Locate every blood parasite and identify its species.
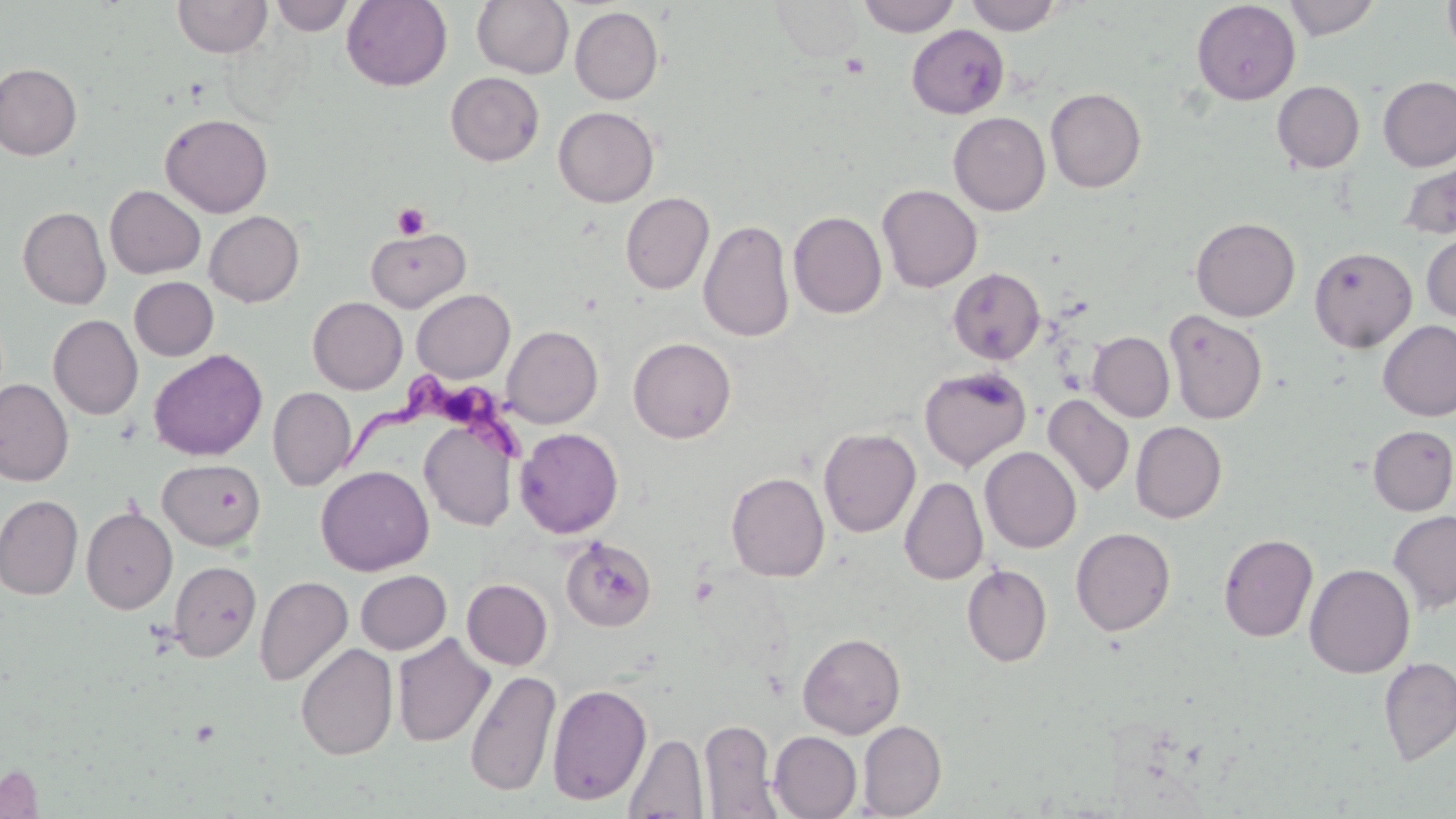

Approximate bounding boxes as [x1, y1, x2, y2] in pixels.
Trypanosoma brucei: [340, 373, 530, 470].
No Plasmodium falciparum, Plasmodium ovale, Plasmodium malariae, Plasmodium vivax, or Babesia divergens observed.

Summary:
  - Uninfected red blood cell locations: [269, 0, 354, 36], [341, 0, 452, 91], [472, 0, 574, 78], [770, 0, 865, 62], [856, 0, 961, 37], [965, 0, 1064, 35], [1283, 0, 1382, 40], [1442, 0, 1456, 60], [172, 1, 272, 58], [1191, 1, 1300, 105], [570, 6, 664, 105], [907, 24, 1009, 118], [0, 62, 82, 161], [445, 72, 545, 166], [1377, 76, 1456, 172], [1272, 81, 1364, 173], [1045, 88, 1146, 192], [553, 106, 659, 207], [948, 112, 1050, 216], [160, 114, 273, 217], [1397, 156, 1456, 240], [877, 184, 982, 292], [105, 185, 206, 279], [125, 185, 215, 361], [620, 192, 714, 294], [17, 206, 111, 309], [203, 211, 305, 307], [789, 211, 886, 318], [1190, 216, 1300, 321], [698, 219, 795, 343], [365, 227, 471, 311], [1421, 230, 1456, 323], [1309, 246, 1417, 352], [948, 268, 1045, 364], [129, 277, 218, 361], [411, 289, 515, 383], [308, 297, 408, 394], [1164, 309, 1268, 424], [48, 314, 143, 420], [1378, 320, 1456, 421], [502, 325, 603, 428], [1088, 332, 1175, 422], [628, 337, 736, 443], [148, 349, 267, 461], [919, 366, 1031, 471], [0, 378, 74, 487], [267, 387, 356, 491], [1043, 394, 1134, 497], [420, 417, 518, 532], [1130, 421, 1226, 523], [1368, 425, 1456, 515], [515, 427, 623, 538], [818, 427, 921, 537], [980, 447, 1081, 553], [158, 458, 266, 550], [316, 465, 434, 576], [726, 472, 830, 582], [899, 477, 988, 585], [0, 495, 83, 600], [81, 506, 177, 614], [1388, 509, 1456, 614], [1071, 527, 1176, 636], [1218, 533, 1318, 642], [560, 537, 657, 632], [168, 561, 262, 661], [1305, 563, 1415, 678], [962, 564, 1052, 667], [355, 570, 451, 654], [254, 576, 353, 687], [462, 578, 552, 670], [798, 632, 906, 739], [392, 633, 495, 747], [296, 643, 398, 761], [1378, 656, 1456, 766], [465, 669, 561, 797], [547, 683, 652, 805], [700, 719, 780, 818], [858, 720, 946, 818], [769, 731, 861, 818], [623, 732, 707, 818], [1, 763, 43, 817]
  - Platelet locations: [840, 53, 869, 78], [392, 203, 431, 240]
  - Slide-level diagnosis: Trypanosoma brucei
  - Modality: optical microscopy
  - Field of view: single
  - Stain: May-Grünwald-Giemsa
  - Preparation: thin blood smear
  - Image size: 1456×819 pixels
  - Magnification: 1000x